Outline platelets.
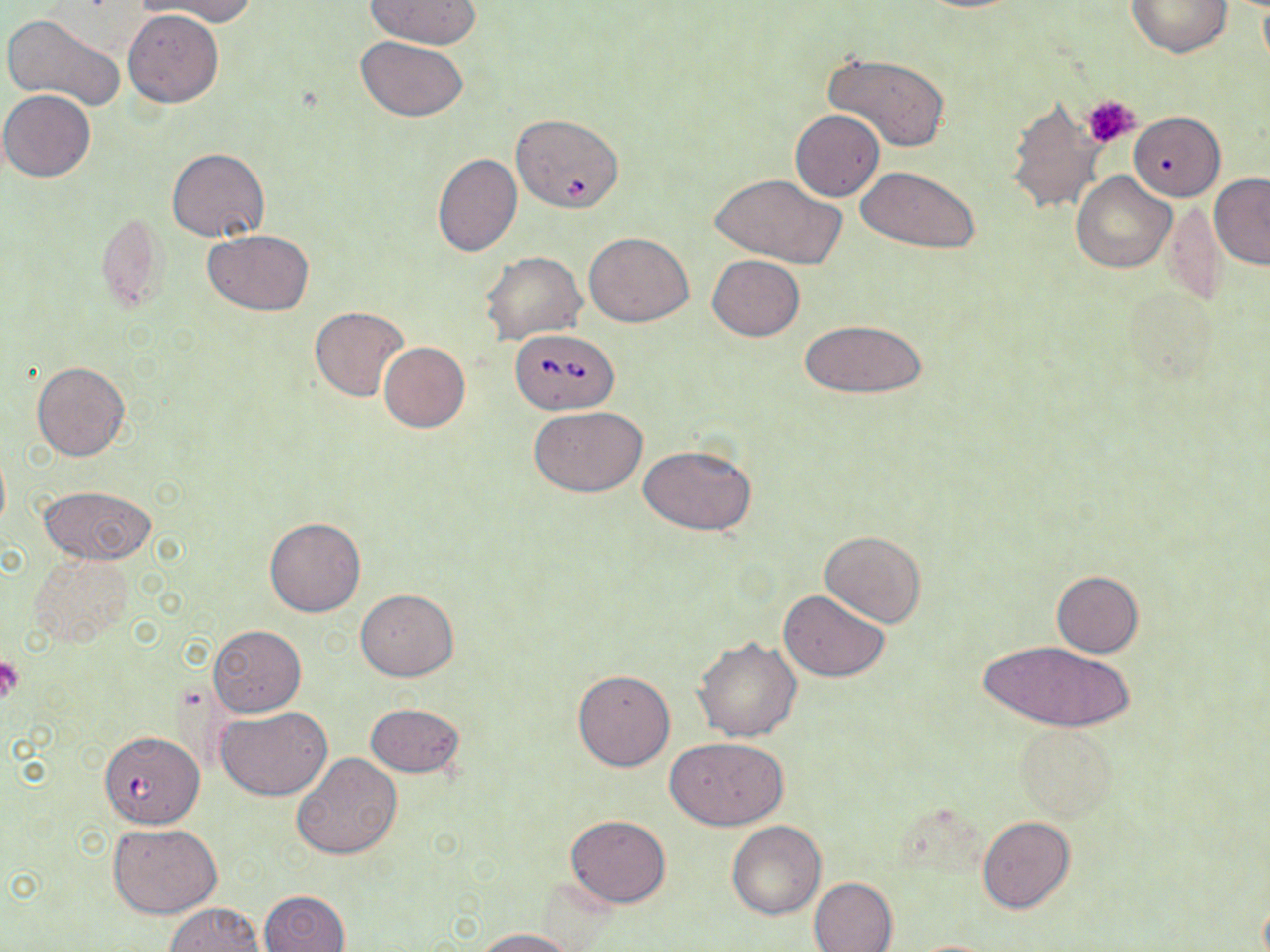
Approximate bounding boxes as [x1, y1, x2, y2] in pixels.
Platelets: [1084, 95, 1140, 148], [0, 657, 24, 702].

Uninfected red blood cell locations: [143, 0, 258, 25], [366, 0, 480, 48], [1125, 0, 1234, 57], [124, 9, 223, 107], [4, 13, 126, 113], [355, 35, 469, 121], [821, 50, 951, 153], [1, 89, 97, 182], [1005, 97, 1106, 215], [790, 111, 884, 200], [1129, 111, 1226, 199], [167, 148, 269, 242], [431, 152, 523, 257], [856, 165, 980, 255], [1070, 171, 1176, 274], [710, 173, 845, 267], [1209, 174, 1270, 269], [1160, 198, 1226, 307], [94, 210, 171, 315], [203, 230, 314, 315], [584, 232, 694, 327], [481, 250, 588, 343], [708, 255, 804, 340], [310, 305, 409, 402], [798, 318, 927, 399], [379, 341, 470, 433], [31, 361, 130, 461], [529, 405, 647, 496], [638, 443, 757, 535], [0, 446, 10, 538], [38, 484, 155, 565], [263, 518, 365, 617], [821, 530, 925, 627], [27, 553, 135, 648], [1051, 571, 1144, 657], [356, 588, 458, 680], [778, 589, 890, 681], [209, 623, 305, 716], [694, 637, 802, 743], [978, 640, 1136, 733], [572, 668, 674, 771], [366, 703, 466, 778], [217, 706, 332, 800], [1014, 724, 1118, 821], [665, 736, 790, 830], [291, 752, 402, 860], [566, 814, 670, 908], [976, 814, 1075, 914], [725, 819, 826, 919], [108, 822, 223, 916], [808, 876, 898, 951], [260, 890, 350, 952], [166, 903, 265, 951], [473, 927, 573, 951], [906, 939, 1007, 952]. Babesia divergens-infected red blood cell locations: [509, 117, 629, 215], [510, 328, 619, 414], [103, 734, 206, 829]. Slide-level diagnosis: Babesia divergens. Captured at 1000x magnification. Thin blood film. Optical microscopy. Single field of view. May-Grünwald-Giemsa-stained preparation. Image is 1270×952 pixels.